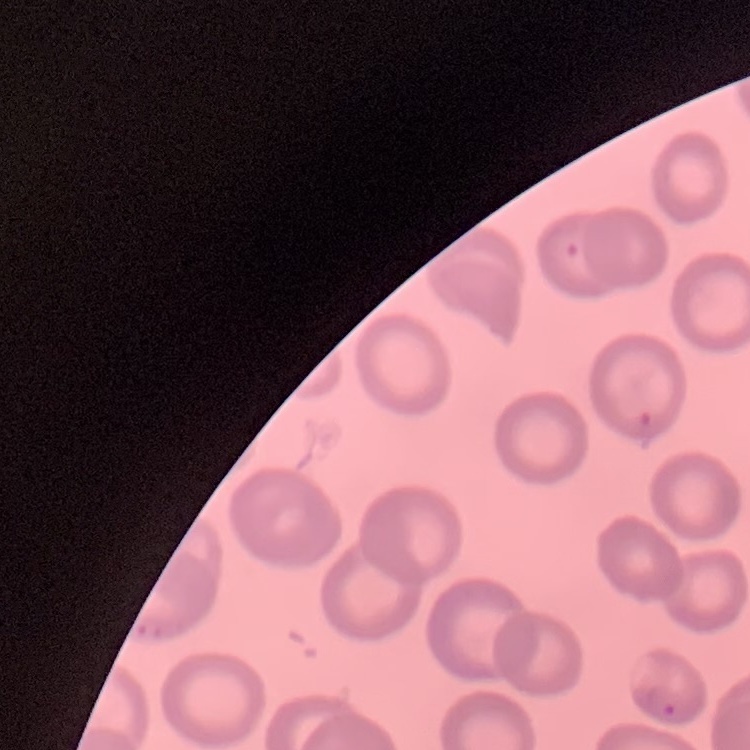

red blood cell morphology = no rouleaux formation
image type = square crop of a larger photomicrograph
preparation = thin peripheral smear
stain = Field's or Giemsa